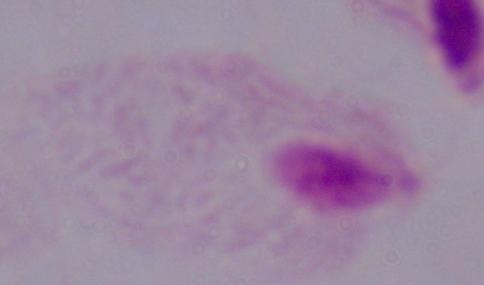
{
  "identification": "trichomonad",
  "modality": "micrograph",
  "magnification": "1000x"
}